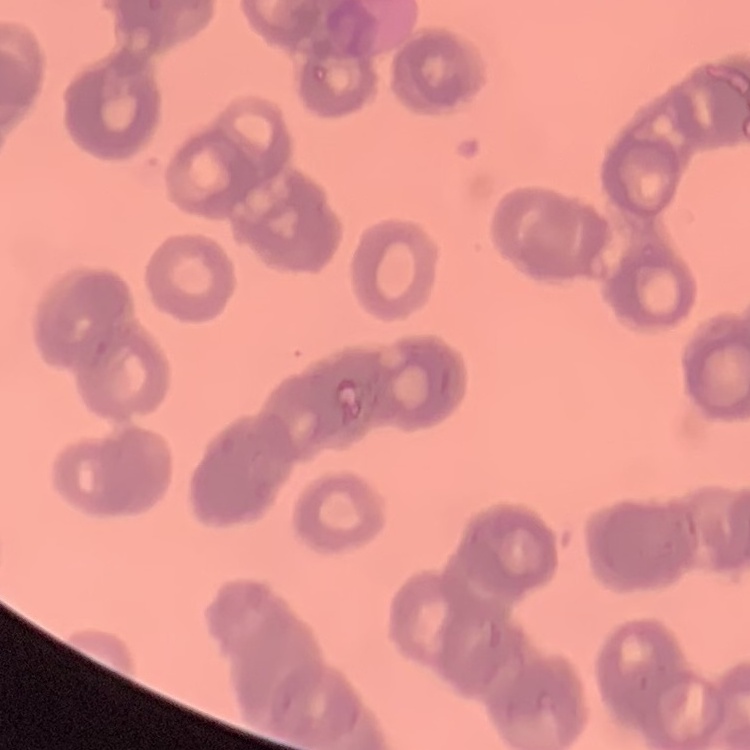
Summary:
  - Red blood cell morphology: rouleaux formation
  - Image type: square crop of a larger photomicrograph
  - Stain: Field's or Giemsa
  - Preparation: thin peripheral smear